State the blood parasite species.
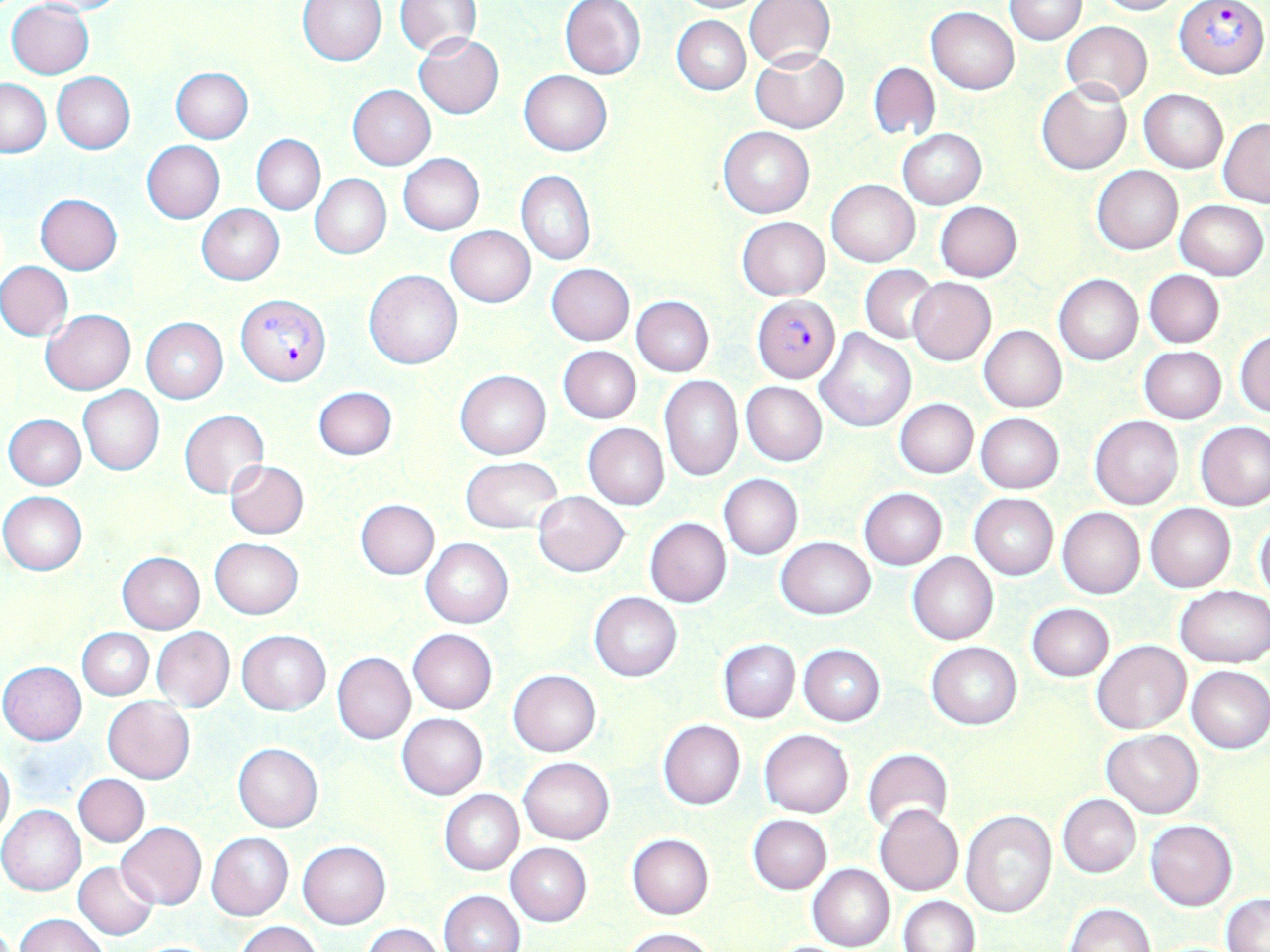

Plasmodium falciparum.

Summary:
  - Coordinate format: approximate bounding boxes as [x1, y1, x2, y2] in pixels
  - Plasmodium falciparum-infected red blood cell locations: [1176, 0, 1268, 79], [234, 294, 331, 386], [753, 296, 840, 383]
  - Uninfected red blood cell locations: [22, 0, 133, 17], [672, 0, 770, 13], [744, 0, 835, 69], [1004, 0, 1086, 44], [1092, 0, 1182, 16], [6, 1, 95, 79], [297, 1, 387, 65], [394, 1, 483, 56], [560, 1, 646, 80], [926, 7, 1019, 95], [671, 15, 750, 95], [1060, 21, 1153, 104], [414, 33, 504, 119], [751, 49, 848, 133], [868, 61, 939, 141], [169, 67, 253, 143], [520, 70, 612, 155], [52, 73, 135, 154], [0, 78, 51, 157], [1037, 80, 1131, 175], [348, 85, 436, 170], [1139, 89, 1228, 173], [1219, 119, 1270, 207], [718, 126, 814, 218], [898, 129, 985, 209], [252, 134, 325, 214], [141, 141, 225, 223], [398, 153, 484, 235], [1093, 166, 1183, 254], [517, 170, 596, 266], [311, 175, 391, 259], [827, 179, 920, 266], [35, 193, 123, 274], [1175, 200, 1269, 280], [935, 201, 1022, 282], [197, 204, 285, 285], [737, 217, 829, 299], [445, 225, 536, 307], [0, 261, 73, 340], [546, 264, 634, 345], [860, 265, 937, 344], [363, 269, 462, 370], [1144, 269, 1224, 348], [1054, 274, 1143, 365], [908, 277, 995, 366], [632, 297, 713, 376], [42, 310, 136, 394], [141, 317, 228, 404], [978, 326, 1066, 412], [815, 329, 916, 434], [1234, 329, 1270, 416], [558, 346, 640, 423], [1140, 346, 1226, 424], [456, 371, 550, 459], [659, 376, 743, 481], [741, 382, 827, 466], [78, 386, 165, 475], [312, 386, 397, 460], [895, 399, 979, 479], [179, 409, 270, 500], [976, 413, 1063, 494], [4, 414, 86, 490], [1091, 416, 1184, 510], [1196, 421, 1269, 511], [583, 424, 670, 508], [460, 456, 563, 535], [224, 461, 308, 539], [719, 474, 802, 560], [859, 488, 947, 570], [0, 492, 87, 575], [533, 492, 628, 576], [969, 493, 1058, 580], [355, 499, 440, 579], [1145, 503, 1236, 592], [1056, 507, 1144, 599], [644, 517, 732, 607], [1253, 517, 1270, 601], [776, 536, 875, 619], [210, 537, 303, 619], [420, 539, 513, 629], [908, 552, 998, 645], [117, 553, 205, 634], [506, 584, 580, 665], [1175, 585, 1269, 668], [589, 593, 682, 682], [1026, 602, 1114, 682], [152, 626, 234, 712], [78, 628, 154, 700], [407, 628, 497, 714], [237, 630, 330, 715], [717, 638, 800, 723], [1092, 640, 1191, 734], [926, 642, 1021, 730], [798, 644, 885, 726], [332, 653, 415, 745], [0, 661, 87, 745], [1186, 665, 1270, 753], [508, 669, 601, 756], [103, 697, 194, 784], [397, 713, 488, 800], [658, 719, 744, 810], [759, 729, 853, 818], [1101, 729, 1204, 817], [232, 743, 323, 832], [862, 749, 952, 836], [0, 751, 14, 838], [518, 756, 614, 844], [73, 774, 149, 848], [440, 789, 523, 875], [1057, 794, 1140, 877], [875, 805, 963, 895], [0, 806, 85, 895], [960, 809, 1058, 919], [748, 815, 831, 893], [1145, 819, 1237, 911], [117, 822, 207, 910], [207, 833, 294, 921], [627, 834, 713, 919], [297, 841, 391, 929], [506, 843, 591, 926], [73, 861, 158, 940], [808, 865, 895, 951], [438, 890, 524, 952], [1221, 894, 1270, 952], [898, 896, 980, 951], [1062, 902, 1155, 952], [14, 913, 109, 952], [236, 920, 324, 952], [361, 923, 445, 952], [623, 927, 716, 952]
  - Magnification: 1000x
  - Modality: optical microscopy
  - Stain: May-Grünwald-Giemsa
  - Image size: 1270×952 pixels
  - Field of view: one of a larger specimen
  - Preparation: thin blood film